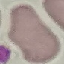

Summary:
  - Malaria status: uninfected
  - Stain: Giemsa
  - Image type: cell patch, automatically extracted from a larger field of view and resized to 64 × 64 pixels
  - Preparation: thin smear
  - Capture: smartphone through the microscope eyepiece